Locate every blood parasite and identify its species.
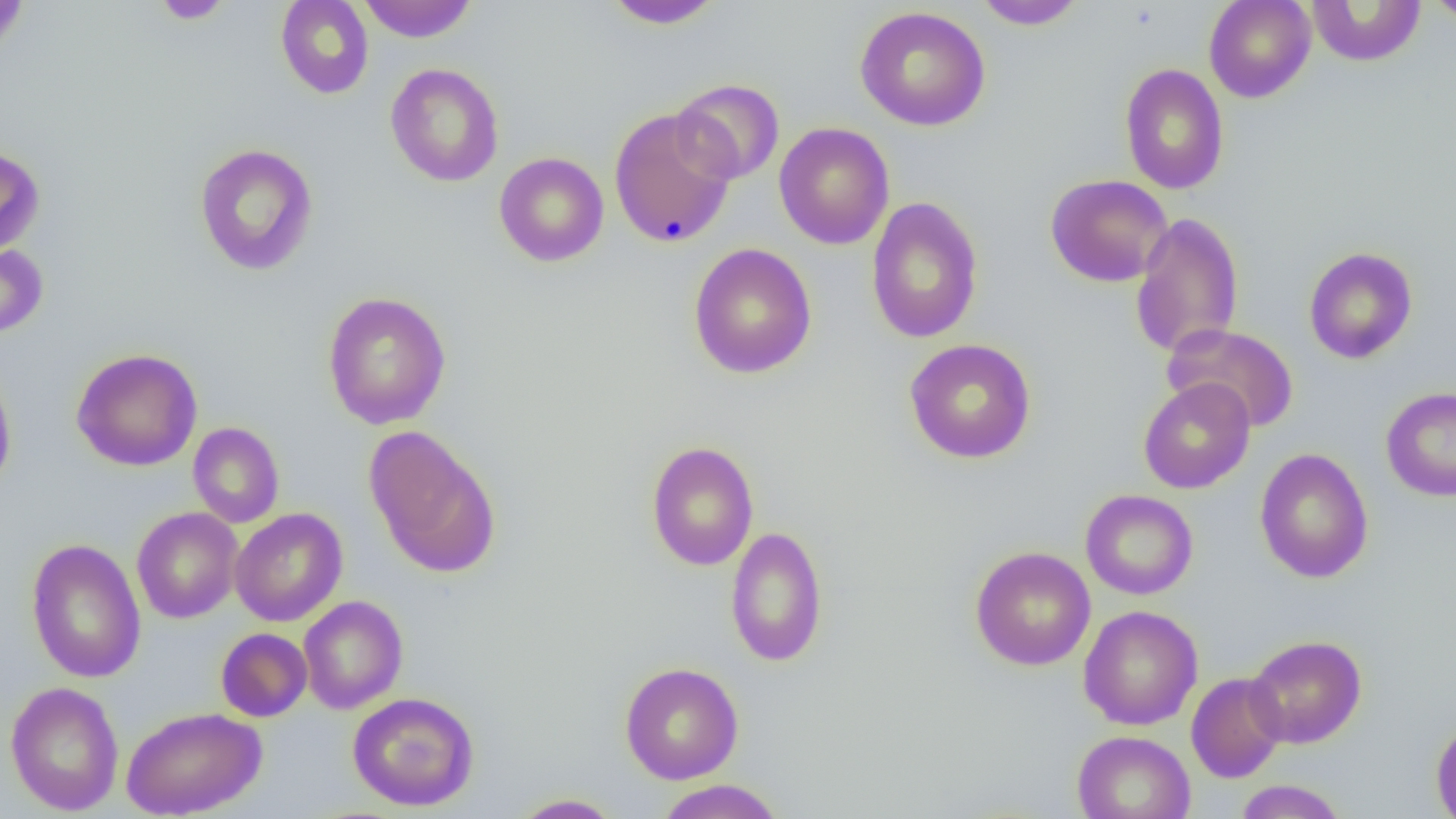

No blood parasites observed.

slide_level_diagnosis: negative for blood parasites
uninfected_red_blood_cell_locations: 'approximate bounding boxes as named x1/y1/x2/y2 corners in pixels: (x1=0, y1=0, x2=29, y2=57), (x1=151, y1=0, x2=233, y2=24), (x1=276, y1=0, x2=374, y2=99), (x1=357, y1=0, x2=478, y2=42), (x1=602, y1=0, x2=725, y2=30), (x1=972, y1=0, x2=1089, y2=30), (x1=1204, y1=0, x2=1316, y2=103), (x1=1425, y1=0, x2=1456, y2=24), (x1=1307, y1=1, x2=1426, y2=67), (x1=854, y1=6, x2=991, y2=131), (x1=385, y1=63, x2=504, y2=187), (x1=1119, y1=63, x2=1230, y2=194), (x1=672, y1=78, x2=785, y2=185), (x1=608, y1=106, x2=738, y2=248), (x1=774, y1=122, x2=894, y2=250), (x1=194, y1=142, x2=318, y2=276), (x1=0, y1=146, x2=44, y2=257), (x1=494, y1=152, x2=609, y2=267), (x1=1045, y1=174, x2=1173, y2=287), (x1=865, y1=196, x2=984, y2=344), (x1=1130, y1=211, x2=1244, y2=360), (x1=0, y1=240, x2=48, y2=340), (x1=688, y1=243, x2=817, y2=379), (x1=1304, y1=247, x2=1417, y2=364), (x1=321, y1=290, x2=452, y2=429), (x1=1162, y1=323, x2=1300, y2=433), (x1=903, y1=338, x2=1037, y2=464), (x1=71, y1=348, x2=203, y2=471), (x1=0, y1=363, x2=16, y2=496), (x1=1138, y1=377, x2=1255, y2=494), (x1=1381, y1=387, x2=1456, y2=501), (x1=188, y1=421, x2=284, y2=528), (x1=364, y1=425, x2=501, y2=575), (x1=645, y1=441, x2=759, y2=571), (x1=1254, y1=448, x2=1373, y2=583), (x1=1080, y1=489, x2=1198, y2=600), (x1=132, y1=506, x2=243, y2=624), (x1=230, y1=508, x2=347, y2=626), (x1=725, y1=526, x2=828, y2=667), (x1=25, y1=537, x2=146, y2=684), (x1=969, y1=546, x2=1096, y2=671), (x1=298, y1=595, x2=408, y2=714), (x1=1078, y1=605, x2=1203, y2=730), (x1=215, y1=627, x2=312, y2=722), (x1=1245, y1=634, x2=1367, y2=749), (x1=620, y1=661, x2=744, y2=784), (x1=1186, y1=672, x2=1288, y2=783), (x1=5, y1=680, x2=124, y2=815), (x1=347, y1=691, x2=480, y2=811), (x1=121, y1=706, x2=267, y2=819), (x1=1431, y1=719, x2=1456, y2=818), (x1=1071, y1=729, x2=1196, y2=819), (x1=654, y1=779, x2=786, y2=819), (x1=1233, y1=780, x2=1349, y2=818), (x1=510, y1=793, x2=626, y2=818)'
magnification: 1000x
preparation: thin blood smear
field_of_view: single
modality: optical microscopy
image_size: 1456×819 pixels